Identify the parasite.
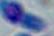

Toxoplasma gondii.

Summary:
  - Modality: micrograph
  - Magnification: 1000x